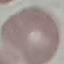
result = no malaria parasites seen
image type = cell patch, automatically extracted from a larger field of view and resized to 64 × 64 pixels
capture = smartphone through the microscope eyepiece
preparation = thin blood smear
stain = Giemsa